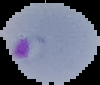

Summary:
  - Image size: 100×85 pixels
  - Malaria status: parasitized
  - Image type: cell region segmented out of the field of view; surrounding area masked to black
  - Preparation: thin blood film